Outline each Plasmodium falciparum-infected red blood cell.
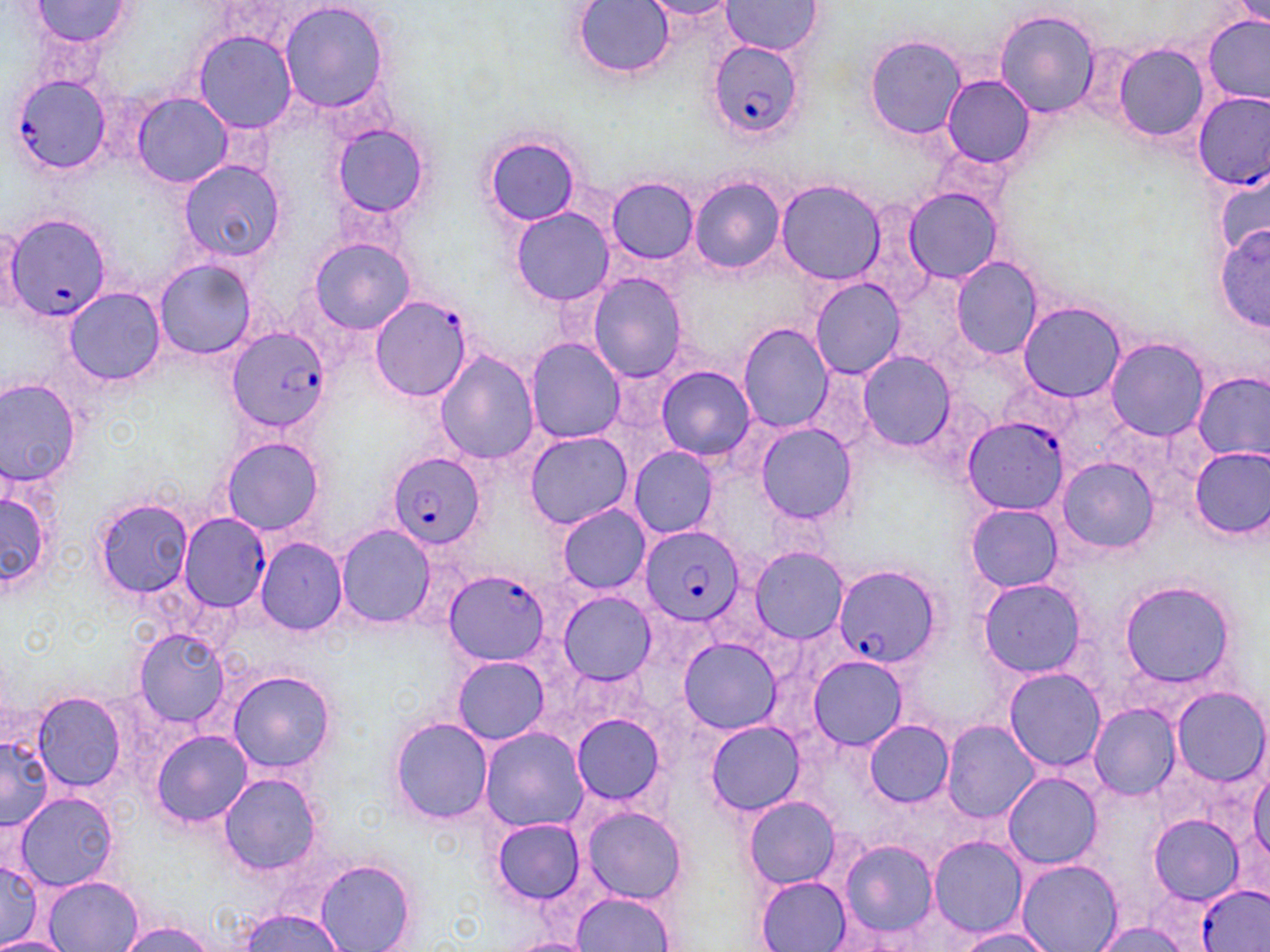
Approximate bounding boxes as (x1,y1)-(x2,y2) corner pairs in pixels.
Plasmodium falciparum-infected red blood cells: (709,42)-(803,142), (11,73)-(112,175), (1193,92)-(1270,188), (4,212)-(113,323), (370,295)-(474,403), (228,329)-(331,434), (963,416)-(1066,517), (387,452)-(484,551), (179,512)-(271,609), (640,527)-(744,627), (830,565)-(940,669), (442,569)-(549,666), (1197,885)-(1270,952).

Summary:
  - Uninfected red blood cell locations: (27,1)-(133,50), (573,1)-(675,79), (640,1)-(740,22), (721,1)-(822,55), (279,2)-(391,114), (993,8)-(1101,117), (1202,15)-(1269,101), (193,30)-(298,134), (867,35)-(964,138), (1115,46)-(1209,142), (940,74)-(1034,168), (132,92)-(234,188), (329,121)-(432,220), (483,134)-(583,225), (180,160)-(285,263), (1213,173)-(1270,254), (689,177)-(784,275), (607,178)-(699,264), (775,180)-(885,284), (903,187)-(1003,283), (511,208)-(615,307), (0,221)-(22,314), (1217,223)-(1270,329), (308,238)-(415,334), (951,256)-(1042,358), (154,260)-(255,359), (588,273)-(688,381), (809,278)-(906,379), (63,287)-(164,387), (1017,303)-(1127,403), (738,324)-(835,434), (1104,337)-(1209,440), (525,338)-(626,443), (434,350)-(539,465), (855,352)-(956,450), (800,365)-(881,460), (657,366)-(755,461), (1192,370)-(1270,462), (0,378)-(81,489), (753,423)-(856,525), (523,432)-(635,529), (219,436)-(326,536), (1188,447)-(1270,541), (628,448)-(719,540), (1054,457)-(1159,554), (0,485)-(60,603), (93,498)-(194,598), (966,504)-(1064,592), (556,505)-(652,593), (335,524)-(435,628), (255,537)-(348,636), (749,546)-(849,643), (1117,578)-(1238,692), (978,579)-(1087,677), (558,592)-(657,684), (132,627)-(232,729), (678,638)-(783,734), (805,655)-(907,750), (450,656)-(550,744), (1004,669)-(1105,770), (228,670)-(336,775), (1171,687)-(1268,786), (31,692)-(127,791), (1087,704)-(1181,799), (571,714)-(665,805), (389,716)-(493,825), (941,719)-(1039,823), (863,720)-(955,807), (705,721)-(804,816), (479,728)-(588,834), (151,730)-(251,828), (0,736)-(53,833), (1249,766)-(1269,865), (1002,771)-(1104,869), (219,773)-(323,877), (11,791)-(123,891), (744,796)-(841,889), (580,805)-(687,903), (1150,810)-(1251,905), (490,819)-(586,906), (928,836)-(1025,937), (833,838)-(944,944), (0,859)-(43,945), (315,860)-(416,952), (1016,860)-(1122,952), (755,875)-(851,951), (43,876)-(143,952), (570,892)-(676,951), (238,907)-(343,950), (1090,918)-(1194,952), (116,920)-(220,952), (952,926)-(1060,951), (0,935)-(68,952), (503,935)-(594,952)
  - Slide-level diagnosis: Plasmodium falciparum
  - Image size: 1270×952 pixels
  - Preparation: thin blood film
  - Stain: May-Grünwald-Giemsa
  - Field of view: single
  - Magnification: 1000x
  - Modality: optical microscopy